Identify the parasite.
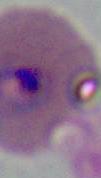

This is Plasmodium.

{
  "magnification": "400x or 1000x",
  "modality": "photomicrograph"
}